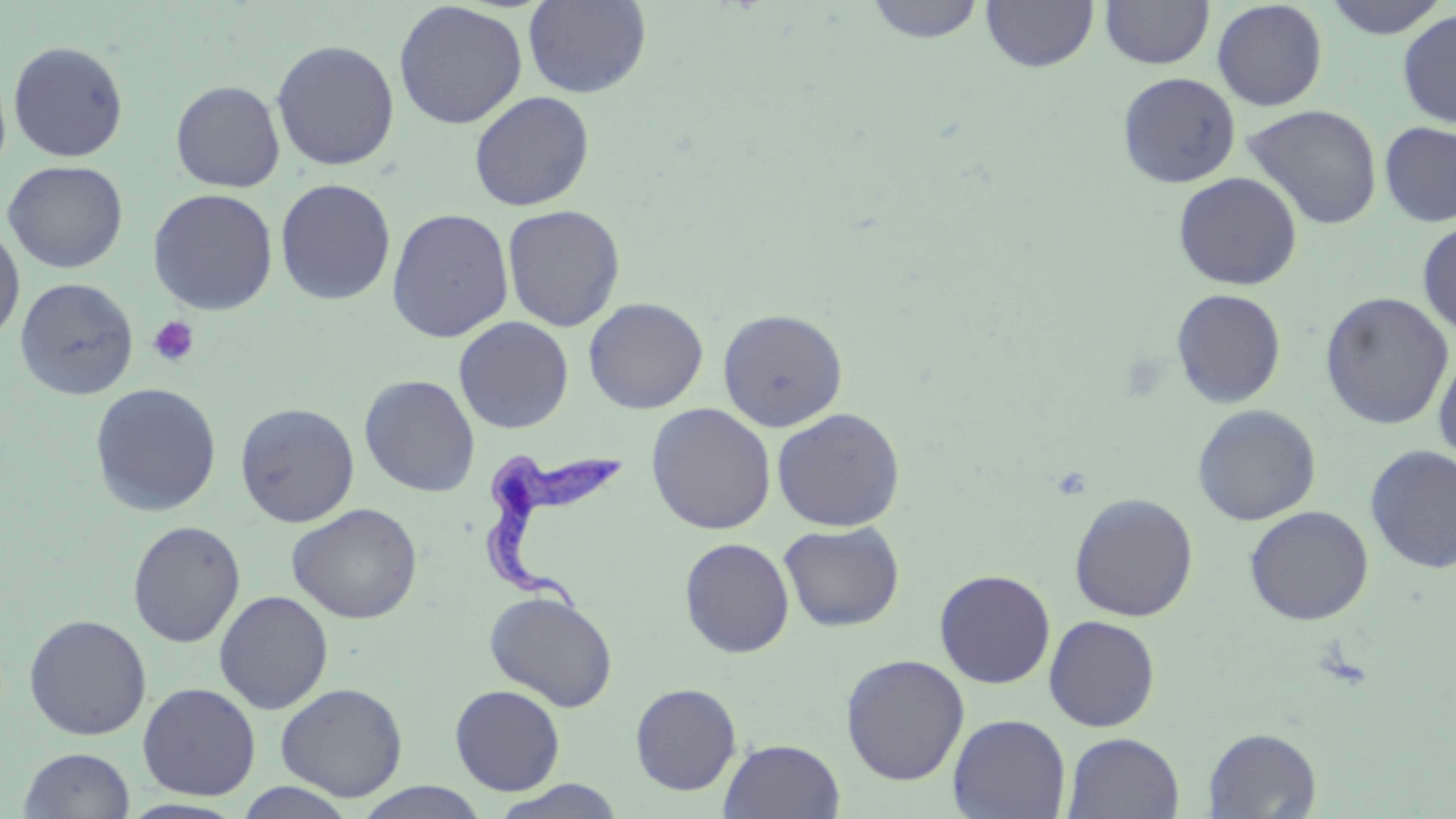 Approximate bounding boxes as named x1/y1/x2/y2 corners in pixels. Platelet locations: (x1=147, y1=315, x2=200, y2=368). Uninfected red blood cell locations: (x1=522, y1=0, x2=652, y2=98), (x1=864, y1=0, x2=986, y2=44), (x1=981, y1=0, x2=1098, y2=72), (x1=1099, y1=0, x2=1215, y2=70), (x1=1321, y1=0, x2=1450, y2=39), (x1=1211, y1=1, x2=1328, y2=111), (x1=393, y1=2, x2=528, y2=129), (x1=1397, y1=9, x2=1456, y2=127), (x1=271, y1=39, x2=400, y2=170), (x1=7, y1=41, x2=129, y2=162), (x1=1117, y1=72, x2=1240, y2=188), (x1=170, y1=80, x2=285, y2=192), (x1=468, y1=90, x2=594, y2=211), (x1=1243, y1=104, x2=1383, y2=230), (x1=1379, y1=121, x2=1456, y2=227), (x1=2, y1=160, x2=129, y2=273), (x1=1173, y1=171, x2=1303, y2=290), (x1=275, y1=177, x2=396, y2=306), (x1=148, y1=188, x2=279, y2=315), (x1=502, y1=204, x2=626, y2=332), (x1=387, y1=208, x2=514, y2=343), (x1=1417, y1=219, x2=1456, y2=337), (x1=0, y1=221, x2=25, y2=345), (x1=15, y1=277, x2=139, y2=400), (x1=1171, y1=289, x2=1287, y2=408), (x1=1319, y1=291, x2=1454, y2=429), (x1=584, y1=297, x2=708, y2=414), (x1=717, y1=308, x2=848, y2=432), (x1=454, y1=316, x2=574, y2=434), (x1=1433, y1=348, x2=1456, y2=467), (x1=359, y1=374, x2=480, y2=497), (x1=89, y1=382, x2=222, y2=516), (x1=235, y1=402, x2=359, y2=527), (x1=646, y1=403, x2=776, y2=534), (x1=1192, y1=405, x2=1321, y2=525), (x1=771, y1=407, x2=906, y2=531), (x1=1365, y1=445, x2=1456, y2=573), (x1=1068, y1=492, x2=1199, y2=621), (x1=287, y1=502, x2=423, y2=624), (x1=1244, y1=505, x2=1374, y2=625), (x1=127, y1=520, x2=246, y2=648), (x1=778, y1=521, x2=905, y2=632), (x1=679, y1=537, x2=795, y2=658), (x1=934, y1=569, x2=1056, y2=689), (x1=214, y1=590, x2=333, y2=714), (x1=483, y1=590, x2=618, y2=711), (x1=23, y1=614, x2=152, y2=740), (x1=1044, y1=615, x2=1161, y2=732), (x1=840, y1=653, x2=969, y2=786), (x1=137, y1=682, x2=260, y2=800), (x1=275, y1=682, x2=408, y2=801), (x1=630, y1=682, x2=742, y2=795), (x1=450, y1=684, x2=566, y2=795), (x1=948, y1=713, x2=1071, y2=819), (x1=1203, y1=727, x2=1322, y2=818), (x1=1062, y1=732, x2=1185, y2=818), (x1=719, y1=738, x2=845, y2=818), (x1=18, y1=747, x2=136, y2=818), (x1=487, y1=779, x2=629, y2=818), (x1=233, y1=782, x2=359, y2=818), (x1=353, y1=782, x2=492, y2=818). Trypanosoma brucei locations: (x1=480, y1=446, x2=630, y2=615). Slide-level diagnosis: Trypanosoma brucei. Captured at 1000x magnification. May-Grünwald-Giemsa stain. Optical microscopy. Thin blood smear. One field of a larger specimen. Image is 1456×819 pixels.